Classify this cell by malaria status.
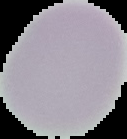

It is uninfected.

Image is 127×139 pixels. Cell region segmented out of the field of view; the surrounding area is masked to black. From a thin blood smear.